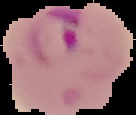

Summary:
  - Preparation: thin blood smear
  - Image size: 136×115 pixels
  - Result: malaria parasites identified
  - Image type: cell region segmented out of the field of view; surrounding area masked to black